Comment on the morphology of the red blood cells.
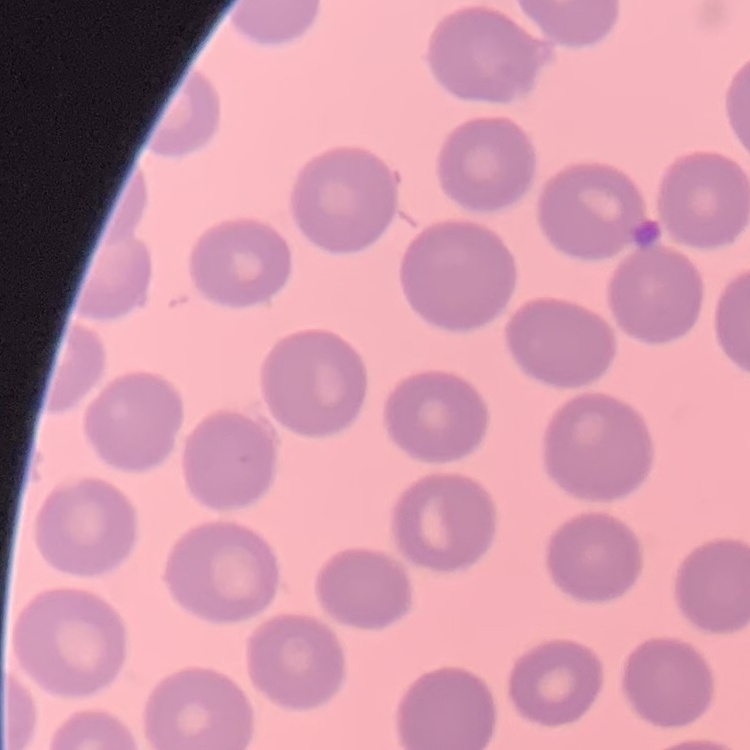

They show no rouleaux formation.

Summary:
  - Stain: Field's or Giemsa
  - Preparation: thin peripheral smear
  - Image type: one tile cut from a larger photomicrograph